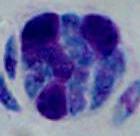
{
  "magnification": "1000x",
  "identification": "white blood cell",
  "modality": "micrograph"
}